Comment on the morphology of the red blood cells.
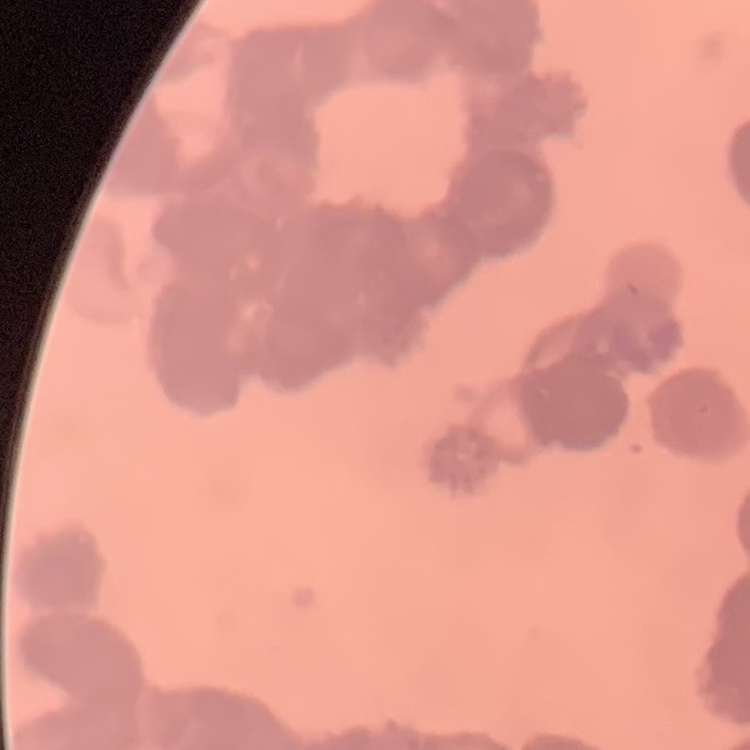
They show rouleaux formation.

Summary:
  - Stain: Field's or Giemsa
  - Image type: one tile cut from a larger photomicrograph
  - Preparation: thin blood smear